Assess this cell for malaria.
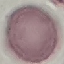
It is uninfected.

image type = automatically extracted cell patch, resized to 64 × 64 pixels
preparation = thin blood film
capture = smartphone through the microscope eyepiece
stain = Giemsa